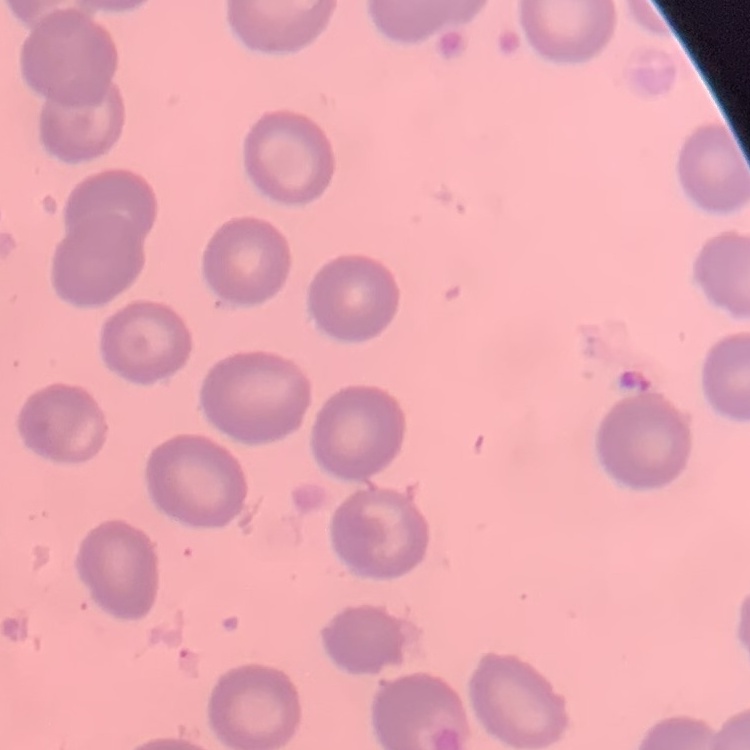

erythrocyte morphology = no rouleaux formation
stain = Field's or Giemsa
image type = square crop of a larger photomicrograph
preparation = thin blood film